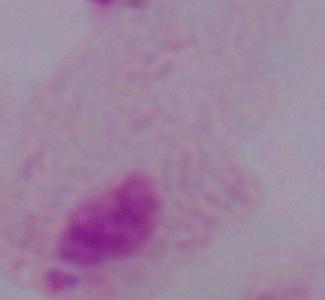
A trichomonad is shown. Micrograph. 1000x magnification.